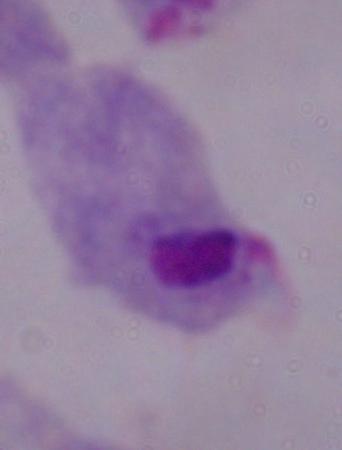
identification: trichomonad
magnification: 1000x
modality: photomicrograph